Outline each Plasmodium malariae-infected red blood cell.
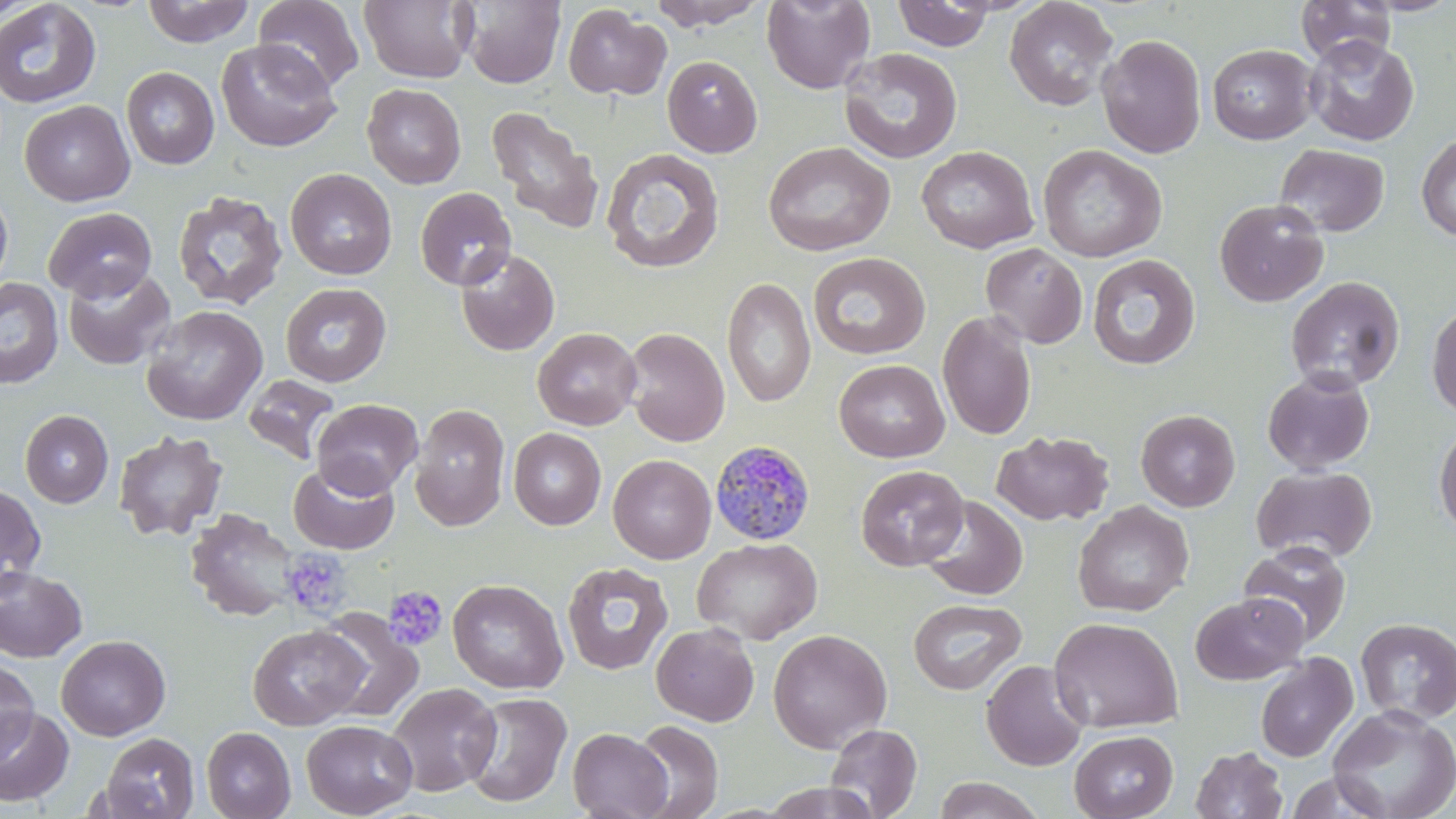

Approximate bounding boxes as (x1,y1)-(x2,y2) corner pairs in pixels.
Plasmodium malariae-infected red blood cells: (709,440)-(815,546).

Uninfected red blood cell locations: (0,0)-(46,23), (142,0)-(255,47), (254,0)-(365,94), (358,0)-(477,84), (461,0)-(565,88), (648,0)-(768,29), (762,0)-(876,95), (1004,0)-(1119,112), (1359,0)-(1456,16), (892,1)-(999,51), (1295,1)-(1397,67), (0,2)-(102,110), (562,5)-(670,100), (1096,34)-(1207,159), (1303,35)-(1419,146), (216,38)-(341,152), (1207,44)-(1317,144), (839,47)-(963,164), (662,55)-(763,157), (121,66)-(219,169), (362,83)-(466,189), (20,100)-(135,206), (485,107)-(604,233), (1416,133)-(1456,243), (762,141)-(895,257), (1275,143)-(1390,237), (1038,144)-(1166,262), (916,145)-(1039,253), (601,147)-(725,274), (285,169)-(397,280), (0,187)-(13,295), (415,187)-(516,291), (172,191)-(287,311), (1214,198)-(1328,307), (43,207)-(157,302), (981,243)-(1088,349), (455,248)-(560,356), (808,252)-(930,359), (1086,254)-(1201,371), (62,266)-(176,370), (1285,276)-(1405,392), (722,277)-(816,407), (0,278)-(63,388), (280,282)-(391,386), (1427,302)-(1456,420), (141,305)-(268,426), (936,311)-(1038,440), (532,327)-(642,430), (623,327)-(729,447), (834,359)-(949,463), (1263,371)-(1375,474), (243,374)-(341,464), (312,399)-(423,497), (410,403)-(510,531), (20,409)-(113,508), (1135,409)-(1240,512), (1433,420)-(1456,540), (508,427)-(606,530), (113,430)-(228,541), (991,430)-(1114,526), (607,454)-(716,564), (288,460)-(400,555), (855,464)-(969,571), (1250,465)-(1377,563), (0,482)-(46,592), (919,496)-(1028,600), (1072,501)-(1194,616), (184,508)-(302,623), (692,537)-(822,644), (1238,540)-(1352,648), (562,562)-(673,675), (0,567)-(87,662), (447,578)-(568,694), (1190,593)-(1308,685), (908,598)-(1027,695), (316,610)-(424,724), (1049,616)-(1183,734), (1355,618)-(1456,725), (651,622)-(760,726), (247,624)-(368,731), (768,628)-(892,752), (56,635)-(171,740), (1255,653)-(1358,763), (981,659)-(1089,771), (0,660)-(38,761), (387,682)-(501,796), (460,691)-(572,808), (1326,703)-(1456,819), (0,707)-(74,806), (301,719)-(417,818), (630,720)-(723,818), (825,723)-(922,818), (201,726)-(296,819), (567,727)-(672,819), (1069,730)-(1178,819), (100,732)-(199,819), (1189,746)-(1288,819), (932,776)-(1045,819), (759,782)-(884,818). Platelet locations: (280,548)-(352,620), (384,586)-(448,652). Slide-level diagnosis: Plasmodium malariae. Image is 1456×819 pixels. Thin blood smear. May-Grünwald-Giemsa stain. One field of a larger specimen. 1000x magnification. Light microscopy.